Give the extent of all Plasmodium falciparum-infected red blood cells.
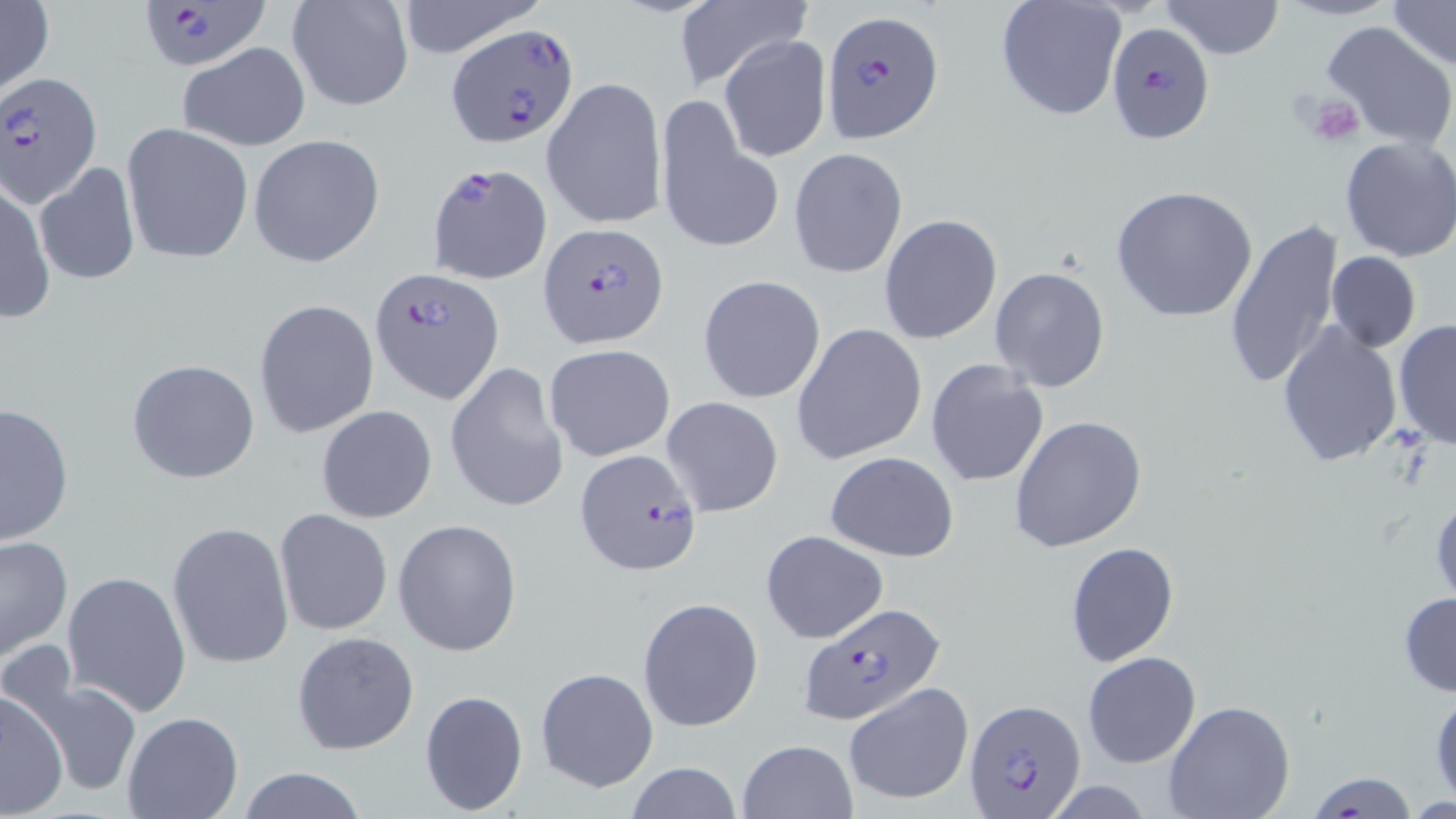
Approximate bounding boxes as named x1/y1/x2/y2 corners in pixels.
Plasmodium falciparum-infected red blood cells: (x1=137, y1=1, x2=268, y2=73), (x1=822, y1=11, x2=943, y2=140), (x1=449, y1=23, x2=578, y2=146), (x1=1107, y1=23, x2=1214, y2=145), (x1=2, y1=71, x2=104, y2=207), (x1=428, y1=162, x2=552, y2=284), (x1=538, y1=222, x2=667, y2=349), (x1=369, y1=265, x2=503, y2=404), (x1=575, y1=448, x2=702, y2=576), (x1=798, y1=603, x2=946, y2=726), (x1=963, y1=699, x2=1086, y2=814).

Summary:
  - Uninfected red blood cell locations: (x1=0, y1=0, x2=54, y2=100), (x1=285, y1=0, x2=414, y2=113), (x1=671, y1=0, x2=811, y2=95), (x1=994, y1=0, x2=1127, y2=122), (x1=1161, y1=0, x2=1285, y2=59), (x1=1277, y1=0, x2=1400, y2=22), (x1=1385, y1=0, x2=1455, y2=70), (x1=392, y1=1, x2=544, y2=57), (x1=1320, y1=18, x2=1456, y2=150), (x1=719, y1=35, x2=830, y2=163), (x1=178, y1=42, x2=311, y2=151), (x1=543, y1=74, x2=667, y2=232), (x1=656, y1=96, x2=772, y2=252), (x1=121, y1=122, x2=254, y2=265), (x1=249, y1=135, x2=385, y2=268), (x1=1337, y1=135, x2=1456, y2=263), (x1=789, y1=147, x2=908, y2=279), (x1=34, y1=161, x2=140, y2=286), (x1=1, y1=178, x2=54, y2=324), (x1=1111, y1=184, x2=1260, y2=324), (x1=879, y1=214, x2=1003, y2=342), (x1=1224, y1=218, x2=1345, y2=390), (x1=1326, y1=250, x2=1420, y2=352), (x1=989, y1=267, x2=1109, y2=392), (x1=699, y1=274, x2=826, y2=403), (x1=254, y1=299, x2=380, y2=438), (x1=1394, y1=320, x2=1455, y2=449), (x1=1276, y1=322, x2=1403, y2=470), (x1=792, y1=323, x2=925, y2=464), (x1=543, y1=343, x2=677, y2=461), (x1=126, y1=357, x2=260, y2=485), (x1=924, y1=360, x2=1049, y2=488), (x1=445, y1=362, x2=568, y2=514), (x1=661, y1=396, x2=785, y2=518), (x1=0, y1=401, x2=73, y2=545), (x1=315, y1=405, x2=437, y2=524), (x1=1010, y1=415, x2=1148, y2=552), (x1=825, y1=452, x2=959, y2=561), (x1=1430, y1=486, x2=1456, y2=609), (x1=275, y1=510, x2=393, y2=635), (x1=394, y1=519, x2=523, y2=657), (x1=167, y1=521, x2=294, y2=670), (x1=761, y1=530, x2=888, y2=644), (x1=0, y1=534, x2=74, y2=663), (x1=1065, y1=541, x2=1179, y2=666), (x1=63, y1=570, x2=192, y2=714), (x1=1397, y1=591, x2=1456, y2=698), (x1=637, y1=596, x2=764, y2=733), (x1=291, y1=631, x2=421, y2=756), (x1=1083, y1=650, x2=1201, y2=768), (x1=536, y1=668, x2=657, y2=792), (x1=30, y1=676, x2=142, y2=798), (x1=1428, y1=681, x2=1455, y2=804), (x1=844, y1=682, x2=975, y2=805), (x1=418, y1=688, x2=530, y2=816), (x1=0, y1=689, x2=69, y2=817), (x1=1162, y1=700, x2=1296, y2=819), (x1=121, y1=712, x2=243, y2=819), (x1=736, y1=738, x2=857, y2=819), (x1=624, y1=762, x2=746, y2=818), (x1=235, y1=767, x2=367, y2=819), (x1=1306, y1=771, x2=1419, y2=817)
  - Platelet locations: (x1=1301, y1=91, x2=1365, y2=148)
  - Slide-level diagnosis: Plasmodium falciparum
  - Field of view: single
  - Modality: light microscopy
  - Preparation: thin blood film
  - Magnification: 1000x
  - Stain: May-Grünwald-Giemsa
  - Image size: 1456×819 pixels